Classify this cell by malaria status.
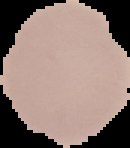

It is uninfected.

Summary:
  - Preparation: thin blood film
  - Image type: cell region segmented out of the field of view; surrounding area masked to black
  - Image size: 130×148 pixels